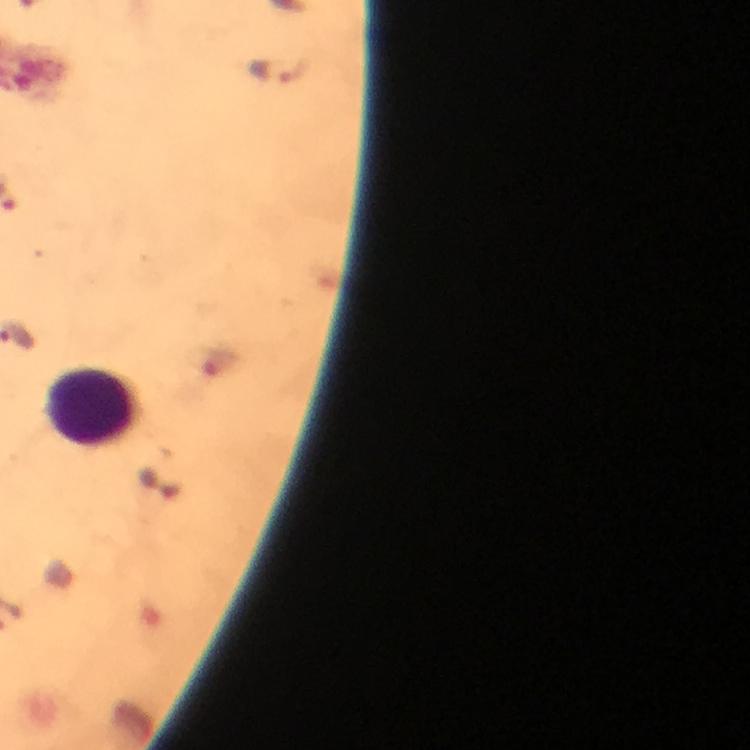

Approximate centers as (x, y) in pixels. Plasmodium parasite locations: (274, 72). Leukocyte locations: (94, 408). Photographed through the microscope with a smartphone camera. Image is 750×750 pixels. Immersion oil was used. At 100x magnification. Giemsa stain. From a malaria diagnostic workup. A crop from one field of view. Thick smear.